Assess this cell for malaria.
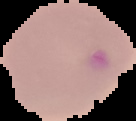
Parasitized.

Summary:
  - Image size: 136×121 pixels
  - Preparation: thin blood film
  - Image type: segmented cell region on a black background